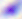

Captured at 400x magnification. Toxoplasma gondii is seen. Photomicrograph.